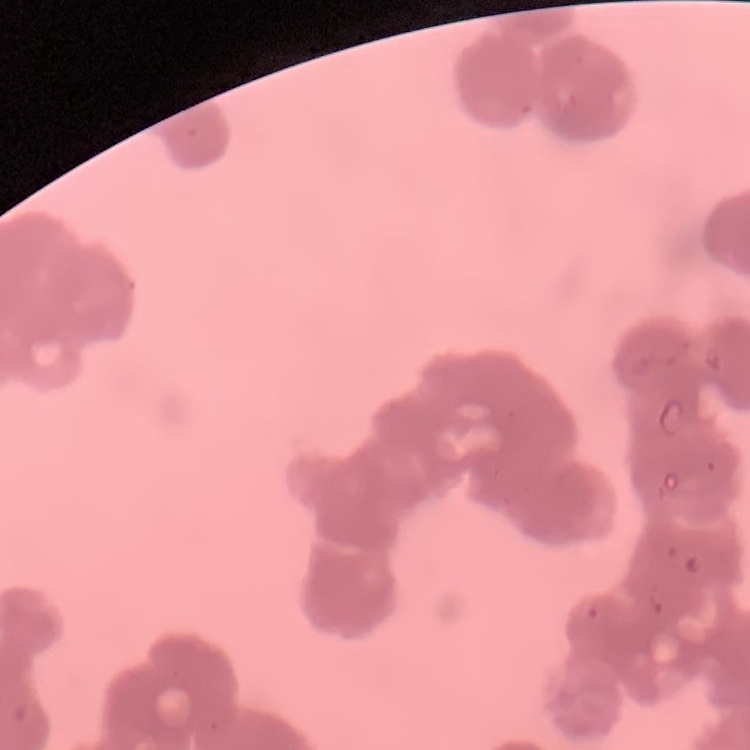

Summary:
  - Erythrocyte morphology: rouleaux formation
  - Preparation: thin blood film
  - Stain: Field's or Giemsa
  - Image type: one tile cut from a larger photomicrograph